Report the malaria status of this cell.
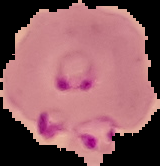

It is parasitized.

Summary:
  - Image size: 160×166 pixels
  - Image type: segmented cell region on a black background
  - Preparation: thin blood smear